Identify the blood parasite species.
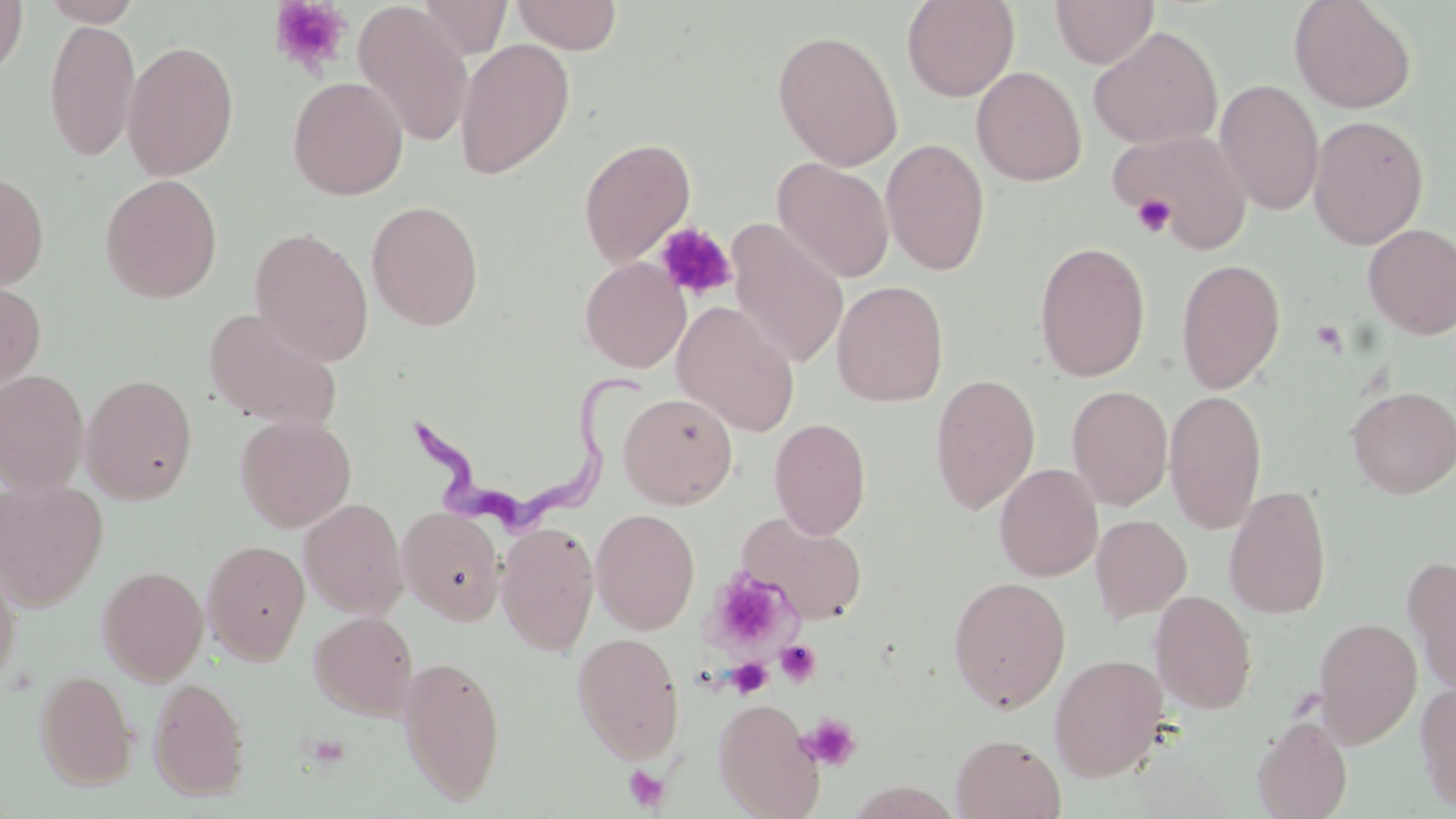

Trypanosoma brucei.

Summary:
  - Coordinate format: approximate bounding boxes as named x1/y1/x2/y2 corners in pixels
  - Uninfected red blood cell locations: (x1=0, y1=0, x2=28, y2=82), (x1=38, y1=0, x2=144, y2=26), (x1=416, y1=0, x2=513, y2=59), (x1=510, y1=0, x2=623, y2=55), (x1=902, y1=0, x2=1019, y2=102), (x1=1050, y1=0, x2=1159, y2=69), (x1=1289, y1=0, x2=1417, y2=114), (x1=353, y1=4, x2=474, y2=148), (x1=44, y1=18, x2=140, y2=163), (x1=1088, y1=26, x2=1223, y2=150), (x1=772, y1=28, x2=904, y2=171), (x1=454, y1=38, x2=575, y2=180), (x1=122, y1=40, x2=239, y2=180), (x1=971, y1=66, x2=1087, y2=187), (x1=287, y1=76, x2=408, y2=201), (x1=1215, y1=79, x2=1323, y2=216), (x1=1307, y1=115, x2=1429, y2=250), (x1=1108, y1=128, x2=1253, y2=250), (x1=578, y1=137, x2=696, y2=268), (x1=880, y1=138, x2=991, y2=276), (x1=773, y1=158, x2=894, y2=282), (x1=0, y1=171, x2=49, y2=291), (x1=99, y1=174, x2=223, y2=303), (x1=366, y1=200, x2=484, y2=330), (x1=727, y1=219, x2=849, y2=370), (x1=1362, y1=224, x2=1456, y2=340), (x1=248, y1=227, x2=374, y2=366), (x1=1033, y1=241, x2=1151, y2=382), (x1=579, y1=256, x2=691, y2=373), (x1=1175, y1=258, x2=1286, y2=394), (x1=0, y1=279, x2=46, y2=398), (x1=831, y1=279, x2=949, y2=407), (x1=671, y1=301, x2=800, y2=436), (x1=204, y1=309, x2=343, y2=431), (x1=0, y1=369, x2=89, y2=492), (x1=80, y1=373, x2=199, y2=504), (x1=930, y1=373, x2=1041, y2=514), (x1=1066, y1=385, x2=1173, y2=509), (x1=1346, y1=385, x2=1456, y2=498), (x1=1163, y1=388, x2=1267, y2=533), (x1=618, y1=392, x2=738, y2=509), (x1=235, y1=415, x2=356, y2=532), (x1=769, y1=417, x2=872, y2=539), (x1=994, y1=463, x2=1103, y2=581), (x1=0, y1=479, x2=108, y2=610), (x1=1223, y1=485, x2=1333, y2=619), (x1=299, y1=498, x2=408, y2=618), (x1=398, y1=506, x2=506, y2=624), (x1=591, y1=508, x2=700, y2=634), (x1=737, y1=510, x2=869, y2=624), (x1=1091, y1=514, x2=1192, y2=623), (x1=496, y1=521, x2=600, y2=656), (x1=202, y1=539, x2=310, y2=665), (x1=0, y1=553, x2=21, y2=690), (x1=1402, y1=555, x2=1456, y2=696), (x1=97, y1=565, x2=209, y2=685), (x1=948, y1=576, x2=1071, y2=713), (x1=1150, y1=590, x2=1257, y2=714), (x1=308, y1=611, x2=418, y2=720), (x1=1314, y1=616, x2=1422, y2=747), (x1=572, y1=632, x2=685, y2=763), (x1=397, y1=653, x2=506, y2=805), (x1=1049, y1=653, x2=1168, y2=781), (x1=35, y1=669, x2=137, y2=790), (x1=148, y1=676, x2=251, y2=800), (x1=1415, y1=680, x2=1456, y2=814), (x1=714, y1=699, x2=825, y2=818), (x1=1252, y1=716, x2=1353, y2=819), (x1=951, y1=733, x2=1065, y2=819)
  - Platelet locations: (x1=269, y1=0, x2=352, y2=76), (x1=1131, y1=193, x2=1175, y2=238), (x1=655, y1=221, x2=738, y2=301), (x1=1309, y1=318, x2=1347, y2=354), (x1=707, y1=569, x2=792, y2=651), (x1=775, y1=641, x2=822, y2=686), (x1=727, y1=656, x2=774, y2=698), (x1=800, y1=712, x2=862, y2=772), (x1=302, y1=732, x2=353, y2=769), (x1=623, y1=765, x2=671, y2=812)
  - Trypanosoma brucei locations: (x1=406, y1=375, x2=645, y2=529)
  - Modality: optical microscopy
  - Magnification: 1000x
  - Stain: May-Grünwald-Giemsa
  - Image size: 1456×819 pixels
  - Field of view: one of a larger specimen
  - Preparation: thin blood smear